State which parasite is depicted.
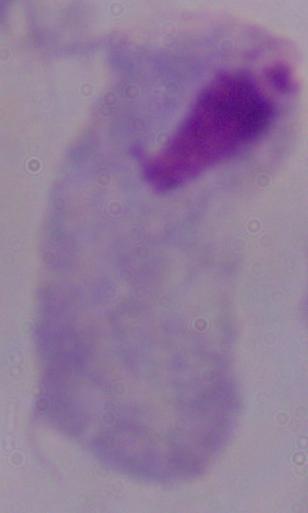

This is a trichomonad.

Captured at 1000x magnification. Photomicrograph.